Describe the morphology of the red blood cells.
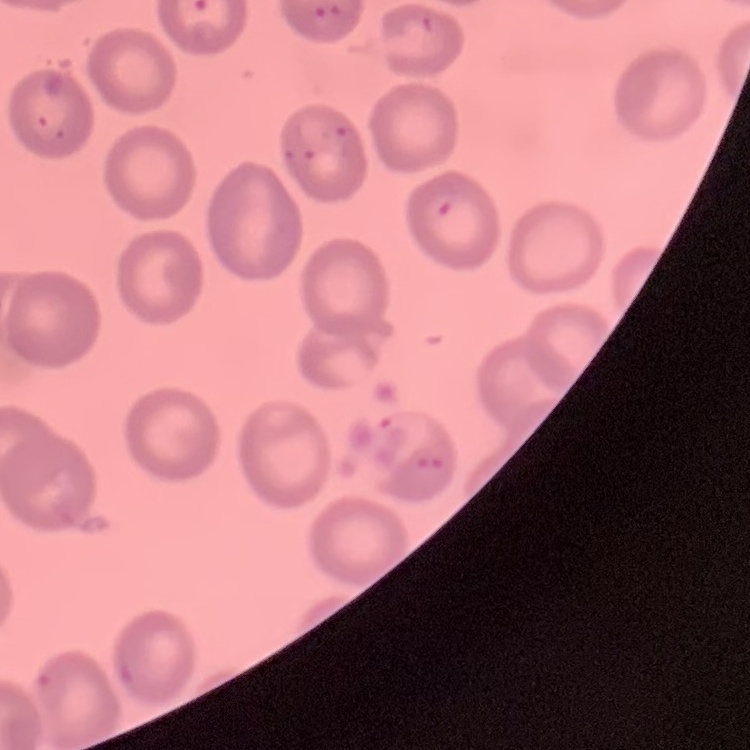
No rouleaux formation.

Field's or Giemsa stain. Square crop of a larger photomicrograph. Thin blood film.